State which parasite is depicted.
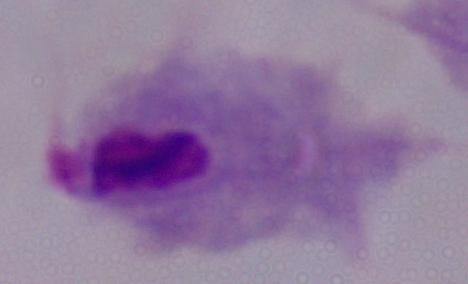

A trichomonad.

Micrograph. 1000x magnification.